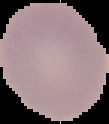
From a thin blood film. Segmented cell region on a black background. Result: negative for Plasmodium parasites. Image is 109×124 pixels.